Name the parasite shown.
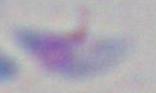
This is Toxoplasma gondii.

1000x magnification. Micrograph.